Assess the morphology of the red blood cells.
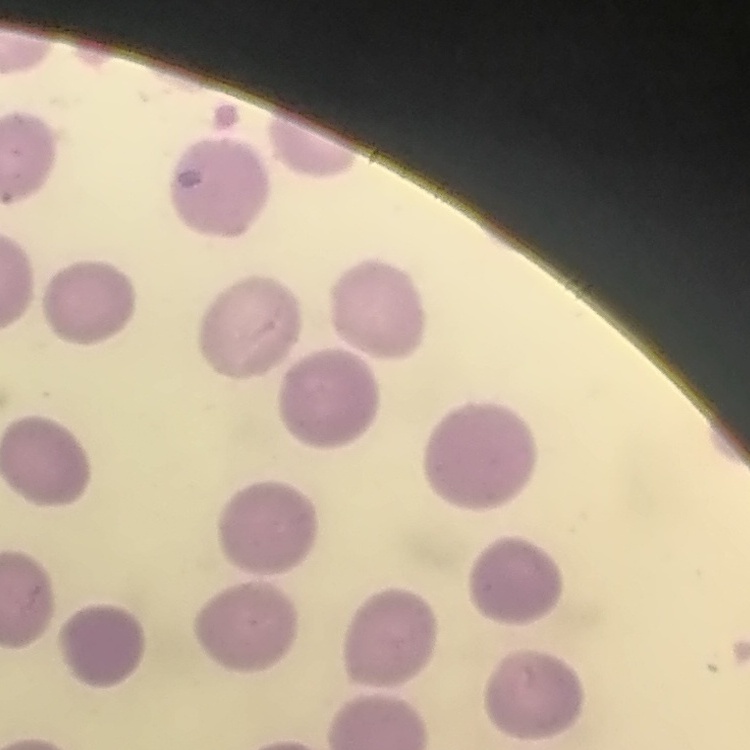
They show no rouleaux formation.

Summary:
  - Stain: Field's or Giemsa
  - Image type: square crop of a larger photomicrograph
  - Preparation: thin blood smear